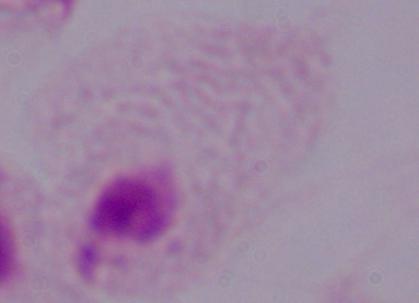

A trichomonad is shown. 1000x magnification. Micrograph.